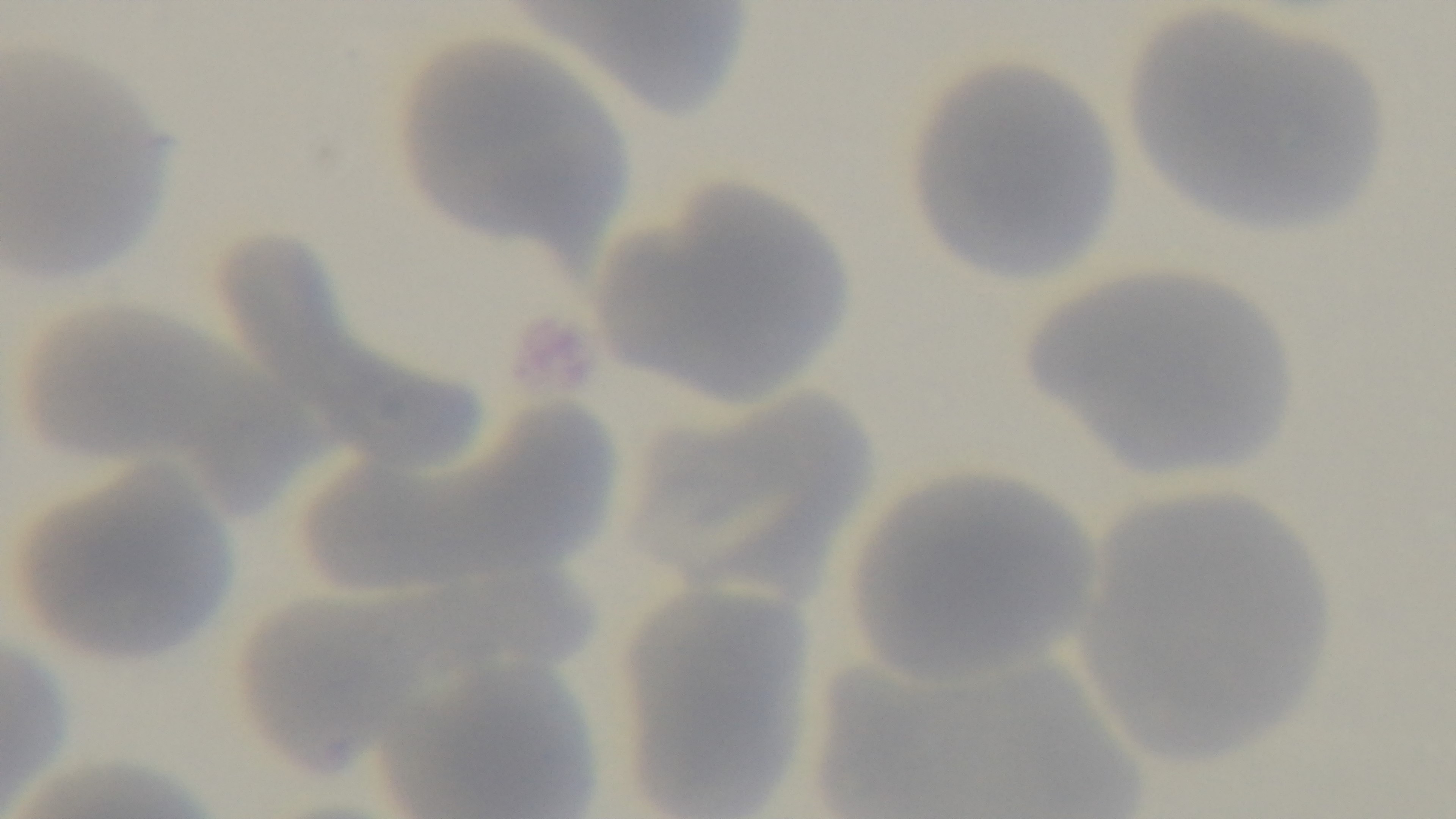

100x oil-immersion objective. Light microscopy. Preparation: thin. Malaria status: uninfected. Captured with a mounted 4K digital camera. Single field of view. Giemsa stain.